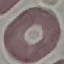

Malaria status: uninfected. Photographed with a smartphone camera at the microscope eyepiece. Thin blood smear. Cell patch, automatically extracted from a larger field of view and resized to 64 × 64 pixels. Giemsa-stained preparation.